Assess this cell for malaria.
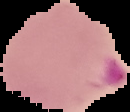

Parasitized.

Image is 130×112 pixels. From a thin blood smear. Cell region segmented out of the field of view; the surrounding area is masked to black.